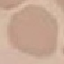
malaria status = uninfected
image type = automatically extracted cell patch, resized to 64 × 64 pixels
capture = smartphone through the microscope eyepiece
preparation = thin blood film
stain = Giemsa